Point out every Plasmodium parasite and every leukocyte.
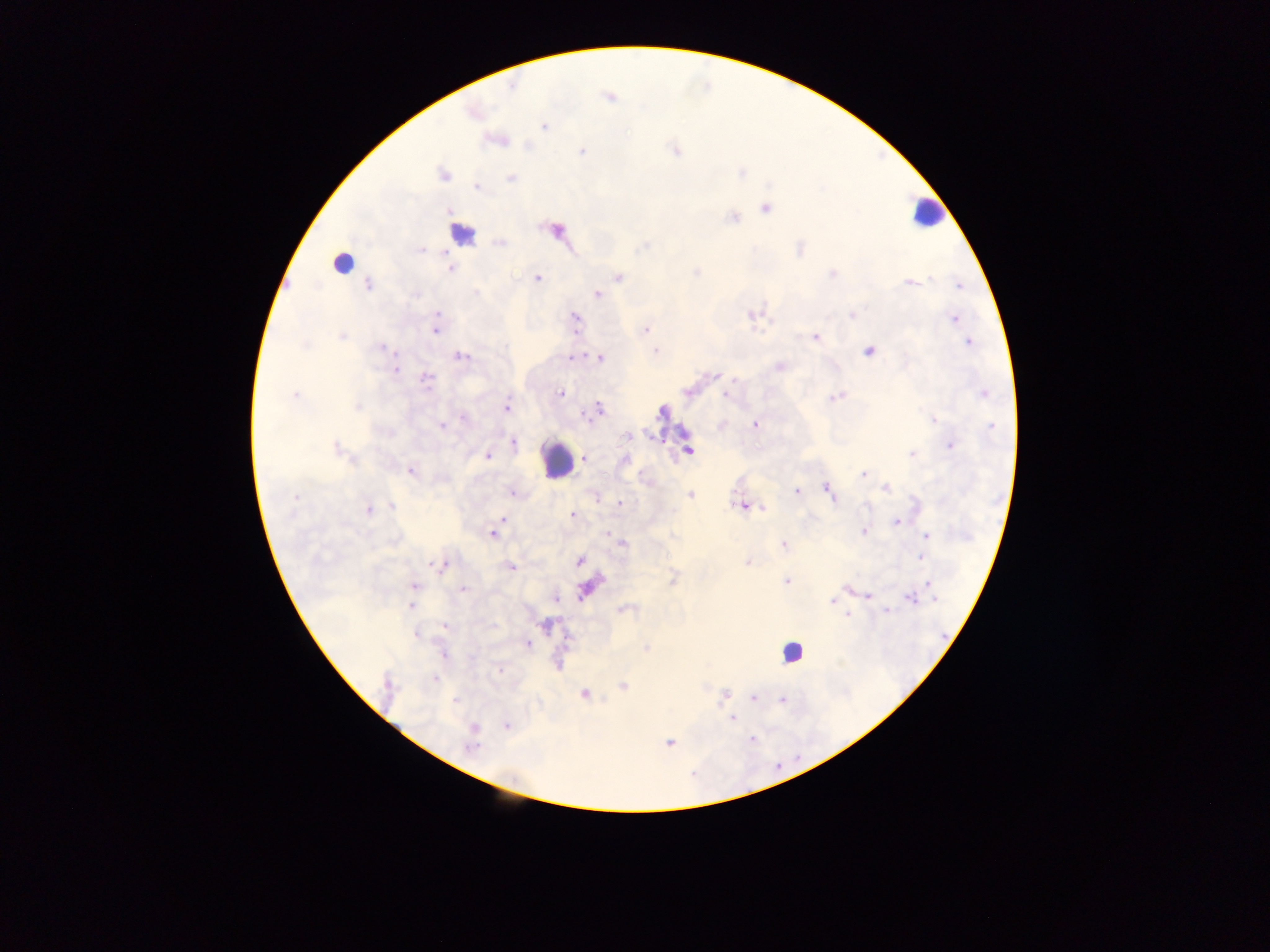

Approximate centers as [x, y] in pixels.
Plasmodium parasites: [512, 86], [609, 97], [543, 127], [675, 150], [581, 151], [444, 175], [510, 179], [477, 187], [766, 209], [449, 210], [733, 218], [557, 230], [500, 243], [645, 246], [799, 248], [421, 251], [450, 269], [696, 272], [832, 273], [537, 278], [618, 278], [930, 280], [909, 282], [368, 284], [959, 285], [598, 294], [415, 295], [437, 315], [751, 315], [852, 315], [576, 318], [955, 319], [435, 331], [646, 331], [341, 336], [814, 336], [968, 343], [304, 347], [384, 348], [656, 350], [869, 352], [461, 356], [572, 357], [599, 358], [779, 367], [395, 371], [716, 375], [426, 380], [734, 380], [687, 392], [560, 393], [984, 394], [726, 395], [294, 396], [835, 397], [357, 407], [506, 408], [599, 409], [661, 412], [463, 418], [934, 420], [756, 425], [441, 426], [992, 428], [627, 436], [512, 443], [950, 445], [337, 448], [688, 450], [911, 454], [488, 457], [585, 458], [410, 471], [863, 475], [887, 488], [829, 490], [796, 491], [512, 493], [691, 494], [295, 497], [597, 499], [620, 503], [392, 506], [741, 506], [763, 508], [674, 509], [368, 510], [572, 514], [502, 519], [896, 522], [863, 531], [608, 533], [493, 534], [927, 537], [623, 542], [783, 544], [921, 557], [579, 561], [747, 563], [439, 565], [510, 567], [673, 580], [786, 581], [928, 584], [414, 587], [847, 588], [463, 589], [584, 590], [869, 595], [911, 598], [556, 599], [935, 599], [832, 601], [411, 605], [623, 610], [887, 611], [847, 616], [444, 626], [416, 635], [528, 644], [646, 649], [443, 654], [499, 669], [435, 680], [623, 686], [584, 693], [724, 695], [753, 698], [455, 700], [781, 700], [732, 719], [506, 726], [473, 728], [752, 739], [669, 744], [471, 747].
Leukocytes (some below the resolvable threshold): [925, 214], [462, 234], [346, 261], [556, 459], [790, 653].

capture = mobile-phone photograph through a microscope
country = Ghana
image size = 1270×952 pixels
preparation = thick blood smear
field of view = single